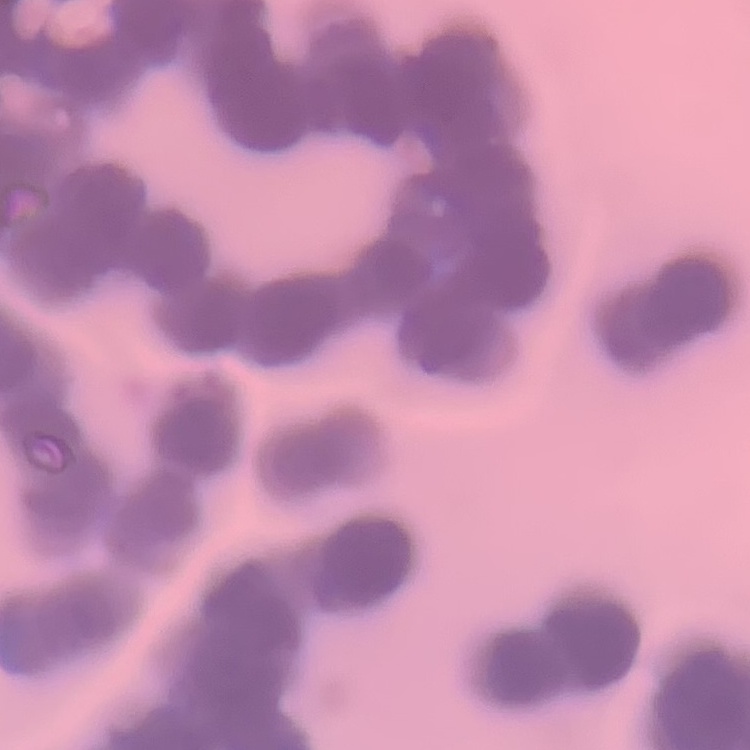

{
  "erythrocyte_morphology": "rouleaux formation",
  "image_type": "one tile cut from a larger photomicrograph",
  "stain": "Field's or Giemsa",
  "preparation": "thin blood smear"
}